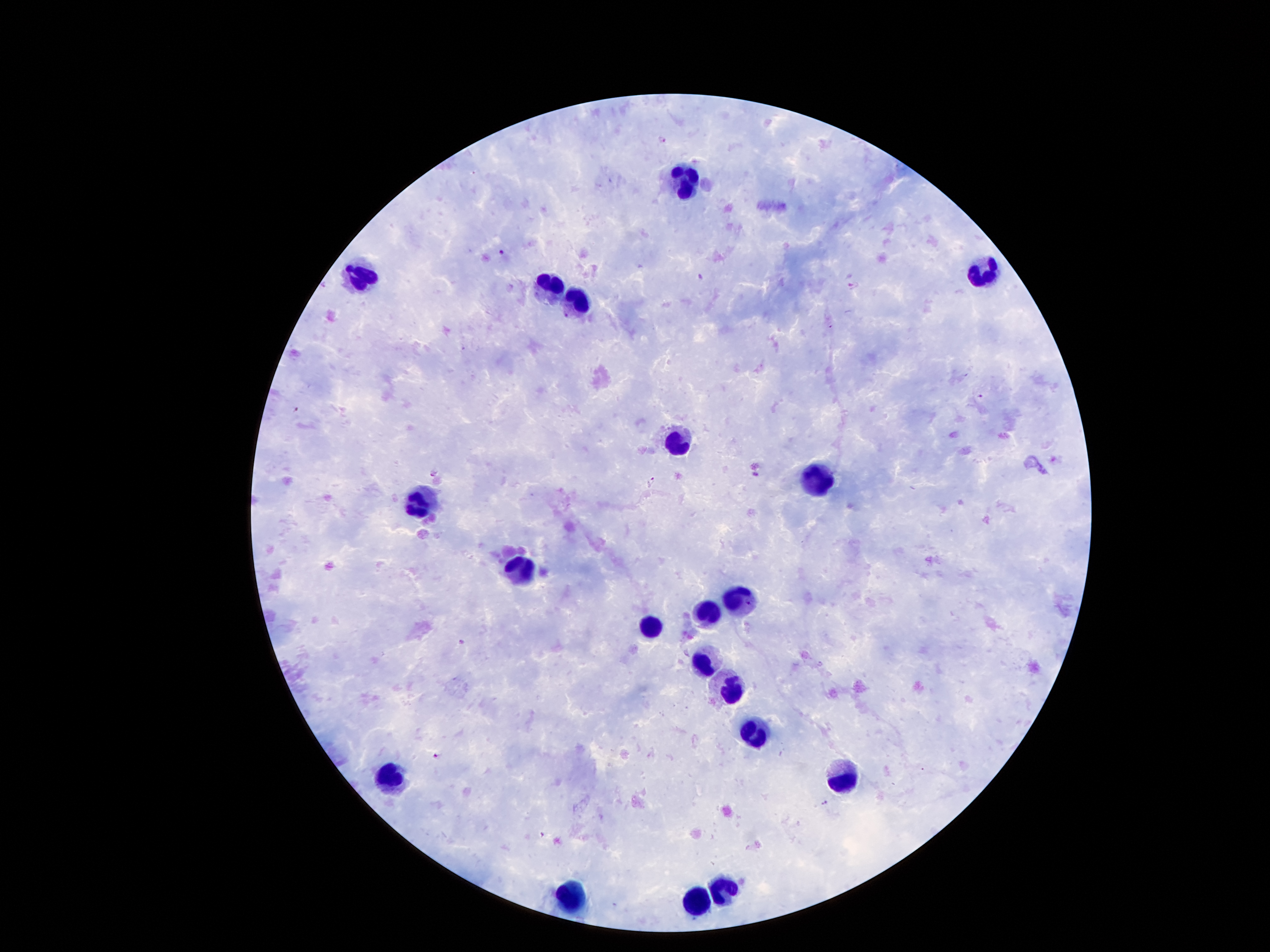
One field from this slide. Thick blood smear. 100x magnification. Giemsa stain. Photographed through the microscope eyepiece with a smartphone camera. Patient malaria status: positive for Plasmodium falciparum. Image is 1270×952 pixels.